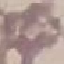

Summary:
  - Malaria status: uninfected
  - Capture: smartphone through the microscope eyepiece
  - Preparation: thin blood smear
  - Image type: cell patch, automatically extracted from a larger field of view and resized to 64 × 64 pixels
  - Stain: Giemsa